Classify this cell by malaria status.
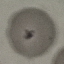

Uninfected.

Giemsa stain. Acquired by smartphone through the microscope eyepiece. Automatically extracted cell patch, resized to 64 × 64 pixels. Thin blood film.